Assess the morphology of the red blood cells.
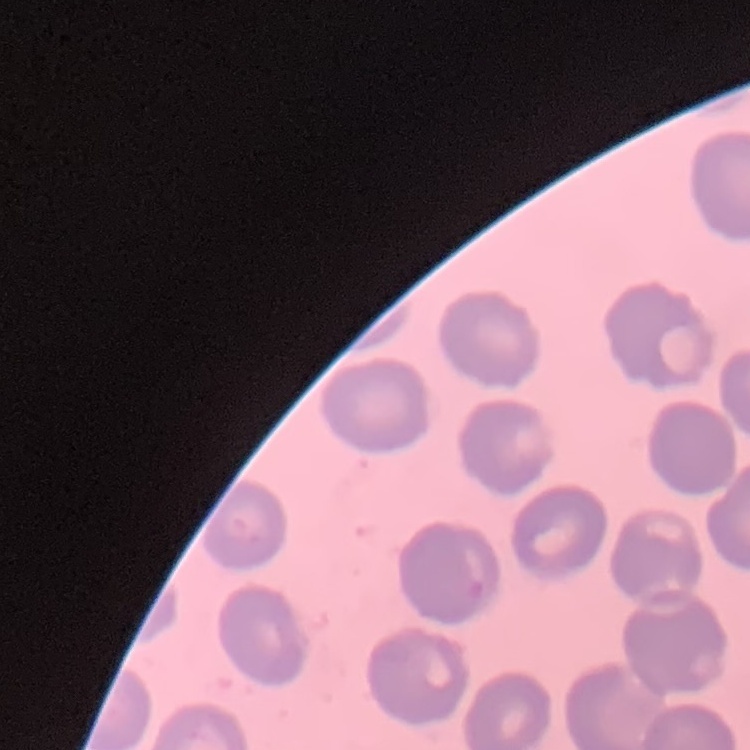
No rouleaux formation.

Summary:
  - Image type: square crop of a larger photomicrograph
  - Stain: Field's or Giemsa
  - Preparation: thin peripheral smear